Assess for parasitized red blood cells.
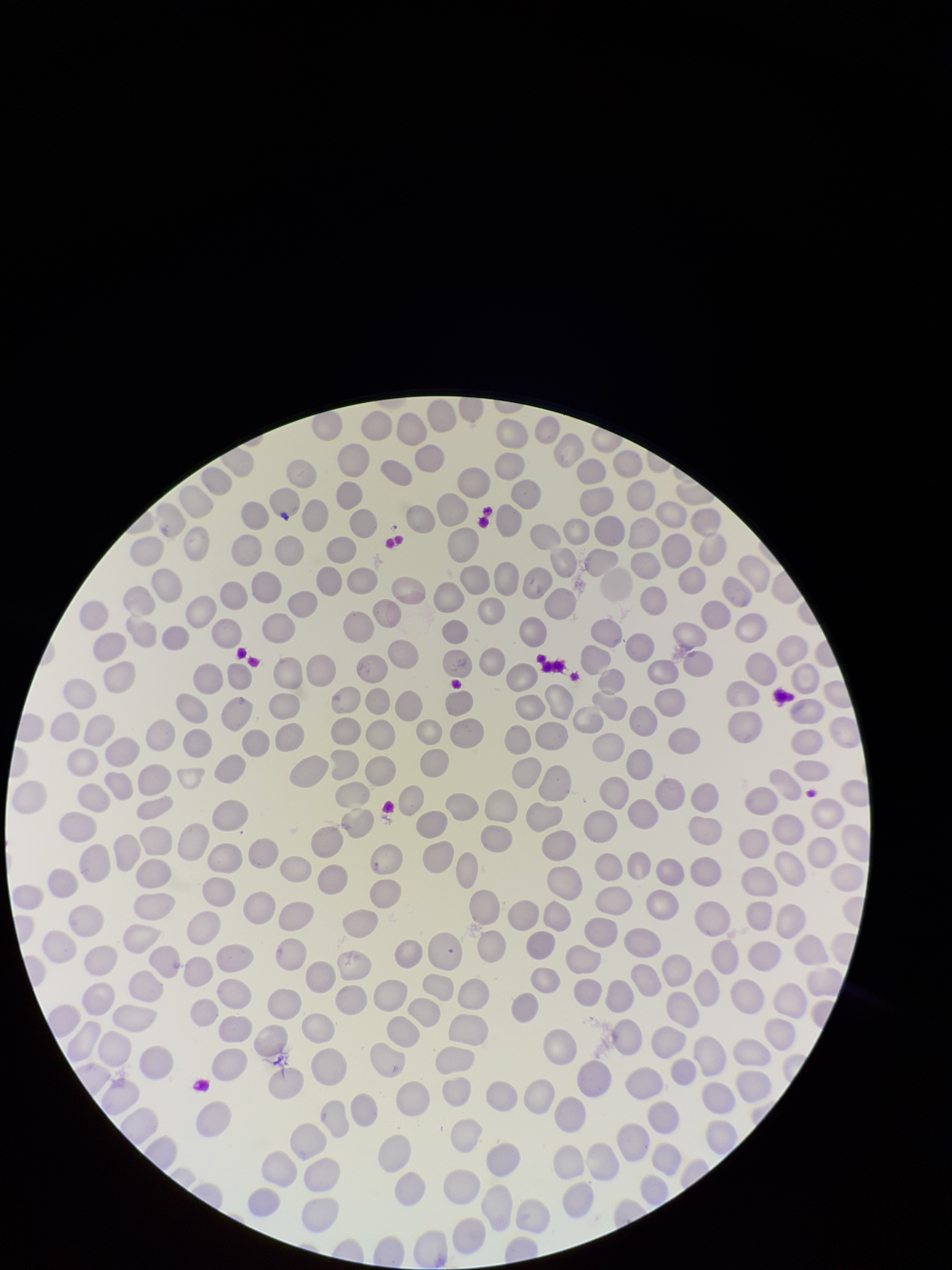
None seen.

parasitized red blood cell count = 0
capture = smartphone photograph through the microscope eyepiece
image size = 952×1270 pixels
stain = Giemsa
field of view = single
preparation = thin blood smear
red blood cell count = 293
patient malaria status = negative